Name the parasite shown.
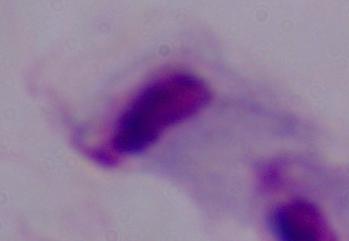

This is a trichomonad.

Summary:
  - Modality: photomicrograph
  - Magnification: 1000x